Describe the morphology of the red blood cells.
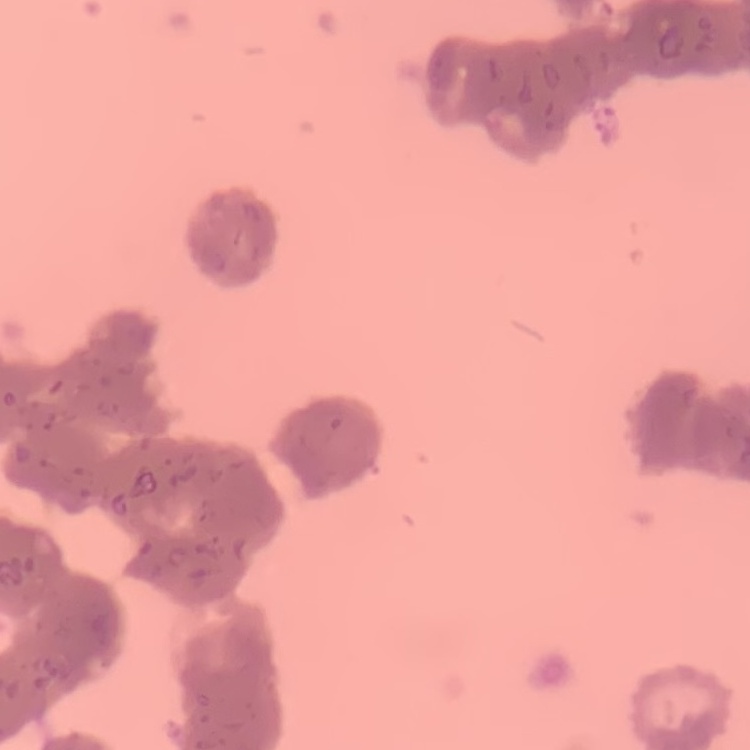

They show rouleaux formation.

Square crop of a larger photomicrograph. Stained with either Field's or Giemsa. Thin blood film.